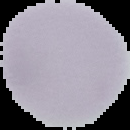

Image is 130×130 pixels. Segmented cell region on a black background. Result: negative for Plasmodium parasites. From a thin blood film.